Name the blood parasite species.
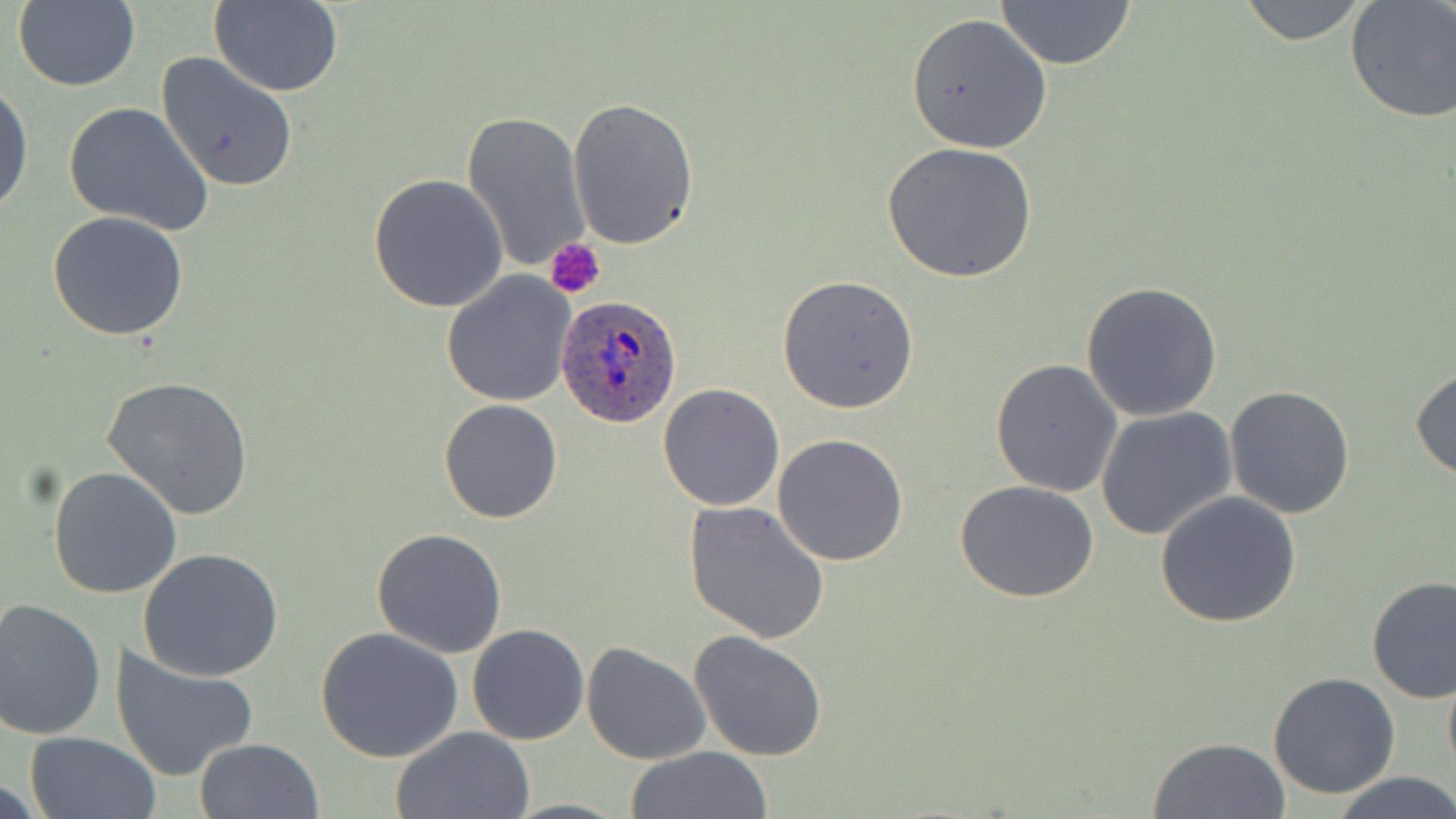

Plasmodium ovale.

Summary:
  - Coordinate format: approximate bounding boxes as named x1/y1/x2/y2 corners in pixels
  - Uninfected red blood cell locations: (x1=11, y1=1, x2=141, y2=92), (x1=210, y1=1, x2=344, y2=96), (x1=994, y1=1, x2=1137, y2=71), (x1=1231, y1=1, x2=1377, y2=46), (x1=1345, y1=1, x2=1456, y2=124), (x1=905, y1=13, x2=1053, y2=155), (x1=154, y1=52, x2=300, y2=194), (x1=0, y1=79, x2=34, y2=219), (x1=568, y1=97, x2=699, y2=250), (x1=62, y1=102, x2=215, y2=237), (x1=462, y1=108, x2=590, y2=273), (x1=881, y1=141, x2=1038, y2=282), (x1=367, y1=173, x2=509, y2=312), (x1=46, y1=212, x2=191, y2=341), (x1=440, y1=273, x2=577, y2=407), (x1=777, y1=274, x2=919, y2=413), (x1=1080, y1=281, x2=1222, y2=421), (x1=990, y1=359, x2=1124, y2=497), (x1=1410, y1=366, x2=1456, y2=481), (x1=100, y1=377, x2=256, y2=522), (x1=658, y1=384, x2=785, y2=510), (x1=1224, y1=385, x2=1356, y2=519), (x1=439, y1=398, x2=563, y2=522), (x1=1096, y1=408, x2=1240, y2=543), (x1=772, y1=433, x2=908, y2=567), (x1=48, y1=466, x2=183, y2=598), (x1=955, y1=481, x2=1101, y2=604), (x1=1154, y1=492, x2=1303, y2=629), (x1=684, y1=499, x2=830, y2=643), (x1=372, y1=529, x2=508, y2=658), (x1=138, y1=549, x2=284, y2=682), (x1=1365, y1=575, x2=1455, y2=703), (x1=0, y1=597, x2=107, y2=742), (x1=467, y1=623, x2=589, y2=746), (x1=315, y1=626, x2=464, y2=763), (x1=687, y1=630, x2=828, y2=762), (x1=581, y1=642, x2=711, y2=766), (x1=110, y1=646, x2=259, y2=781), (x1=1442, y1=659, x2=1456, y2=786), (x1=1267, y1=671, x2=1400, y2=799), (x1=392, y1=726, x2=535, y2=818), (x1=24, y1=732, x2=160, y2=818), (x1=1147, y1=736, x2=1290, y2=818), (x1=193, y1=737, x2=325, y2=819), (x1=623, y1=747, x2=774, y2=819), (x1=1334, y1=772, x2=1456, y2=819)
  - Plasmodium ovale-infected red blood cell locations: (x1=556, y1=296, x2=685, y2=432)
  - Platelet locations: (x1=544, y1=237, x2=604, y2=298)
  - Field of view: one of a larger specimen
  - Preparation: thin blood smear
  - Image size: 1456×819 pixels
  - Modality: optical microscopy
  - Stain: May-Grünwald-Giemsa
  - Magnification: 1000x